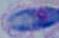

Summary:
  - Identification: Toxoplasma gondii
  - Modality: micrograph
  - Magnification: 1000x